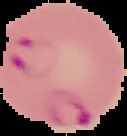

Image is 127×136 pixels. The area outside the segmented cell region is set to black. From a thin blood smear. Result: malaria parasites detected.